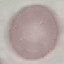
Result: no malaria parasites seen. Cell patch, automatically extracted from a larger field of view and resized to 64 × 64 pixels. Giemsa stain. Thin smear of blood. Photographed with a smartphone camera at the microscope eyepiece.